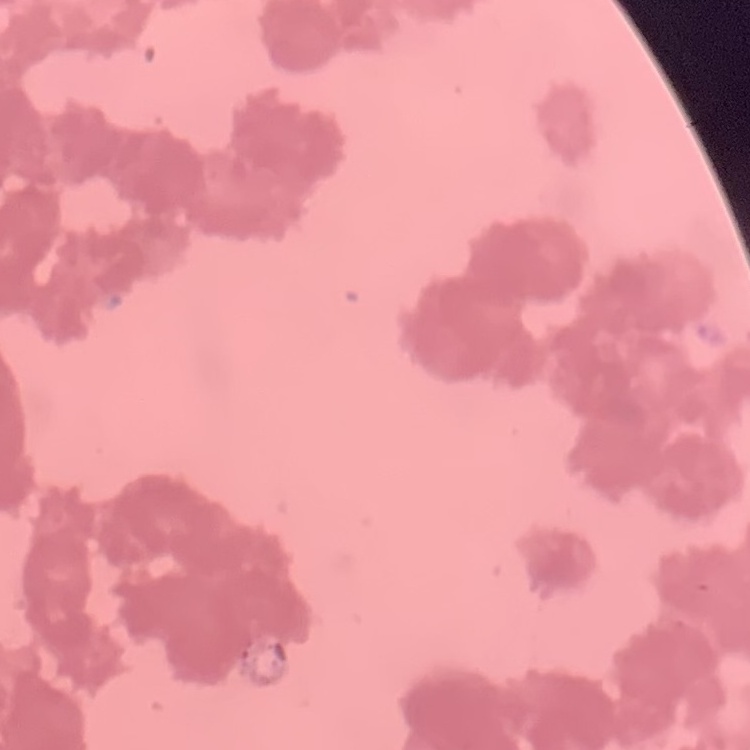
The red blood cells show rouleaux formation. Thin blood smear. One tile cut from a larger photomicrograph. Stained with either Field's or Giemsa.